Identify the parasite.
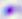
Toxoplasma gondii.

magnification = 400x
modality = photomicrograph